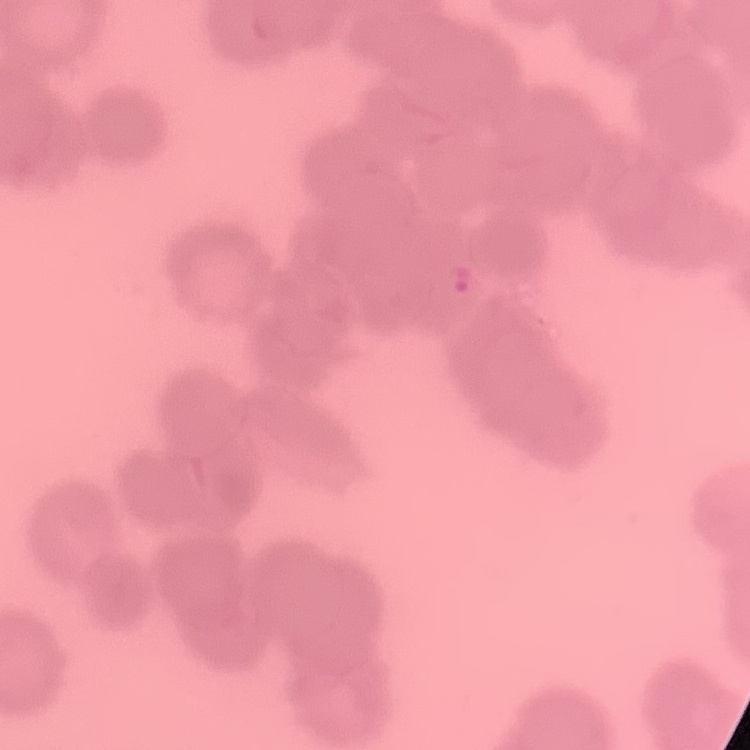

Summary:
  - Erythrocyte morphology: rouleaux formation
  - Image type: one tile cut from a larger photomicrograph
  - Preparation: thin blood smear
  - Stain: Field's or Giemsa